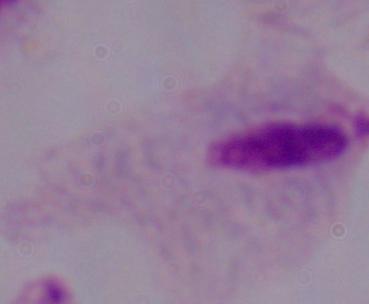 A trichomonad is seen. Micrograph. 1000x magnification.